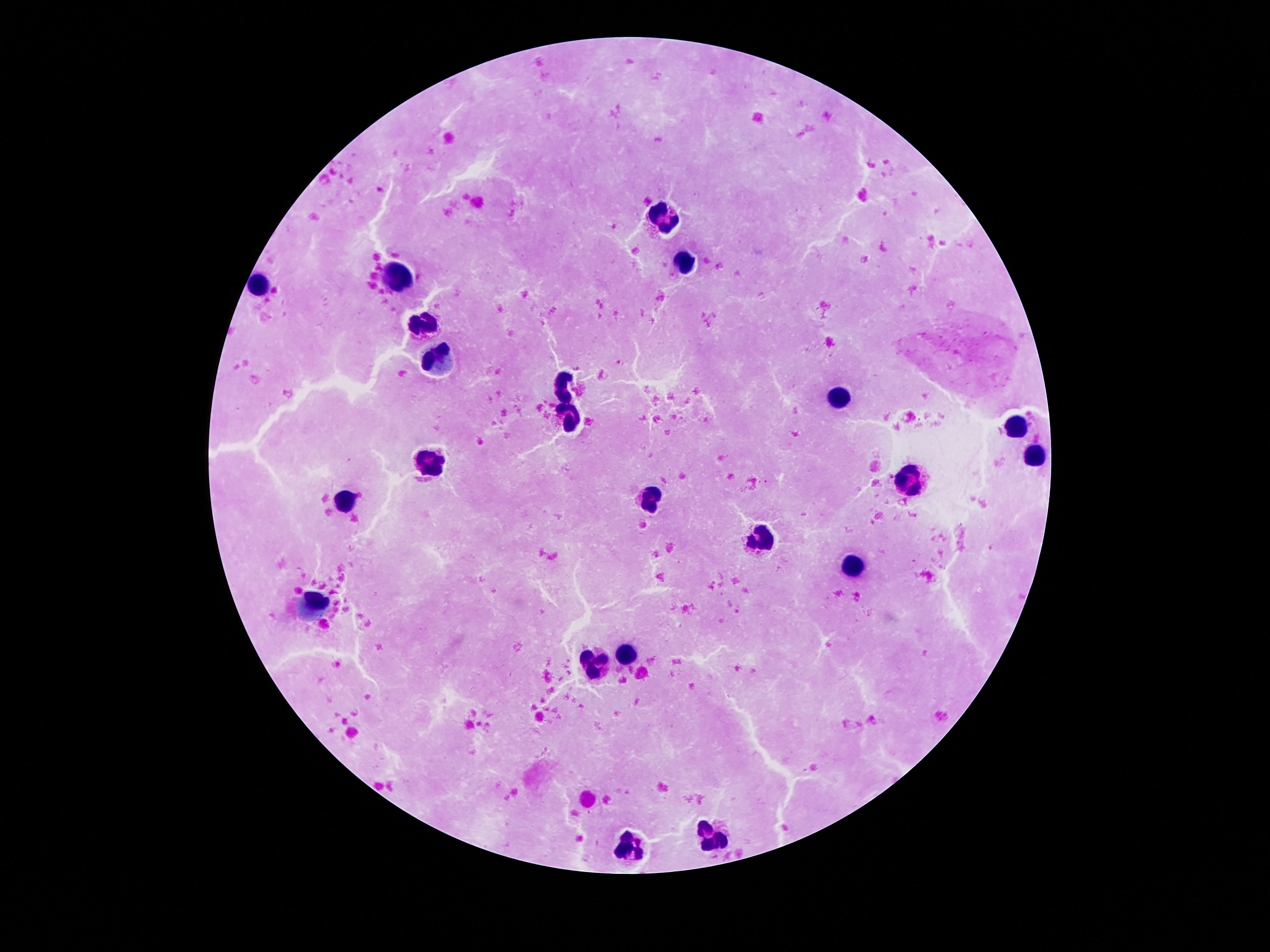

Approximate centers as [x, y] in pixels.
Summary:
  - Leukocyte locations: [664, 221], [688, 262], [397, 275], [260, 283], [422, 322], [438, 357], [563, 385], [838, 398], [568, 418], [1018, 425], [1035, 455], [430, 465], [910, 482], [650, 498], [344, 502], [762, 538], [852, 568], [313, 608], [629, 652], [594, 668], [715, 836], [639, 849]
  - Stain: Giemsa
  - Capture: smartphone camera through the microscope eyepiece
  - Field of view: single
  - Image size: 1270×952 pixels
  - Magnification: 100x
  - Preparation: thick peripheral-blood smear
  - Patient malaria status: not infected